Classify this cell by malaria status.
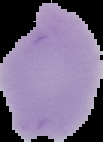

It is uninfected.

{
  "image_type": "cell region segmented out of the field of view; surrounding area masked to black",
  "preparation": "thin blood smear",
  "image_size": "103×142 pixels"
}